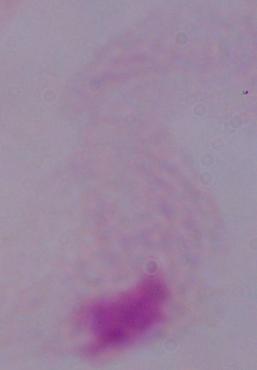
Summary:
  - Magnification: 1000x
  - Identification: trichomonad
  - Modality: micrograph